Identify the cell.
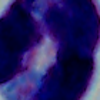

A leukocyte.

magnification = 1000x
modality = photomicrograph